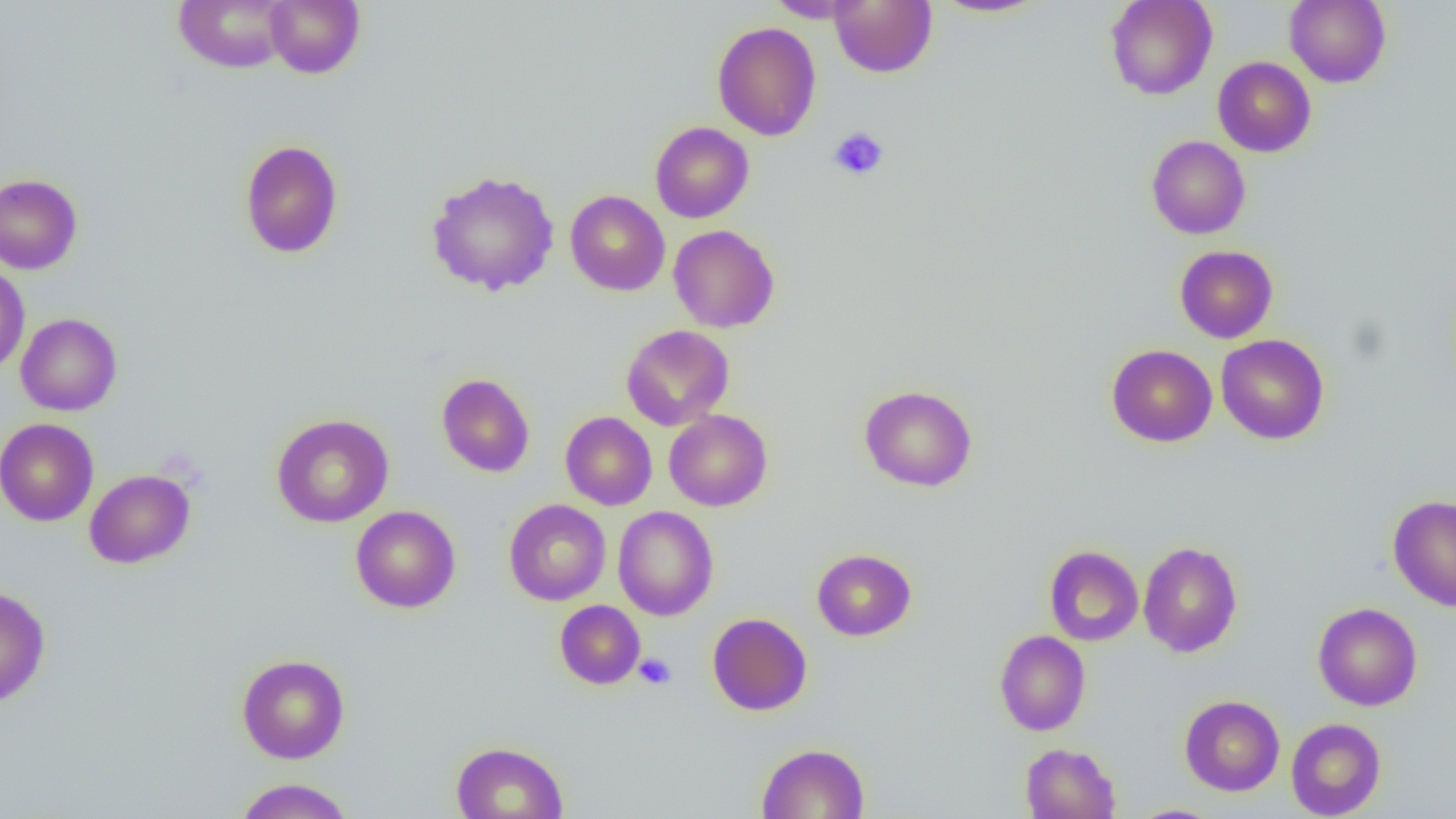

Summary:
  - Coordinate format: approximate bounding boxes as (x1,y1)-(x2,y2) corner pairs in pixels
  - Uninfected red blood cell locations: (173,0)-(293,73), (264,0)-(365,78), (765,0)-(865,22), (829,0)-(937,78), (932,0)-(1049,18), (1105,0)-(1217,100), (1284,0)-(1391,88), (712,22)-(822,141), (1213,56)-(1316,157), (650,122)-(754,223), (1147,135)-(1250,239), (240,139)-(343,259), (426,169)-(560,296), (0,173)-(83,274), (565,191)-(670,296), (668,224)-(780,333), (1175,245)-(1278,343), (0,263)-(30,375), (16,313)-(122,416), (621,324)-(734,431), (1215,334)-(1329,444), (1106,344)-(1217,447), (436,373)-(535,477), (859,385)-(977,491), (664,409)-(772,511), (560,411)-(657,510), (270,413)-(394,527), (0,418)-(99,526), (84,469)-(195,569), (1388,494)-(1456,611), (504,499)-(611,605), (350,505)-(461,613), (613,506)-(719,621), (1138,541)-(1242,657), (1044,545)-(1143,646), (812,549)-(917,641), (0,586)-(50,707), (555,600)-(645,689), (1313,602)-(1422,711), (707,613)-(812,716), (994,630)-(1090,736), (237,654)-(350,763), (1179,694)-(1284,795), (1286,717)-(1386,818), (451,741)-(568,819), (1020,742)-(1121,819), (756,743)-(869,819), (234,778)-(354,818), (1127,804)-(1224,819)
  - Platelet locations: (828,126)-(888,181), (634,652)-(677,690)
  - Slide-level diagnosis: negative for blood parasites
  - Field of view: one of a larger specimen
  - Modality: optical microscopy
  - Preparation: thin blood smear
  - Magnification: 1000x
  - Image size: 1456×819 pixels